Identify the parasite.
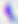
This is Toxoplasma gondii.

Captured at 400x magnification. Photomicrograph.